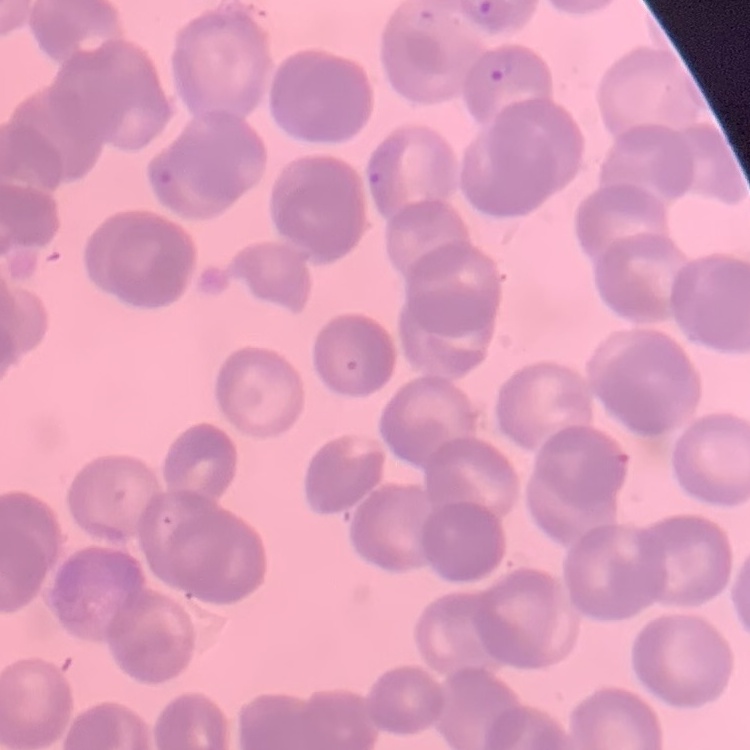

red blood cell morphology = rouleaux formation
preparation = thin blood film
stain = Field's or Giemsa
image type = square crop of a larger photomicrograph